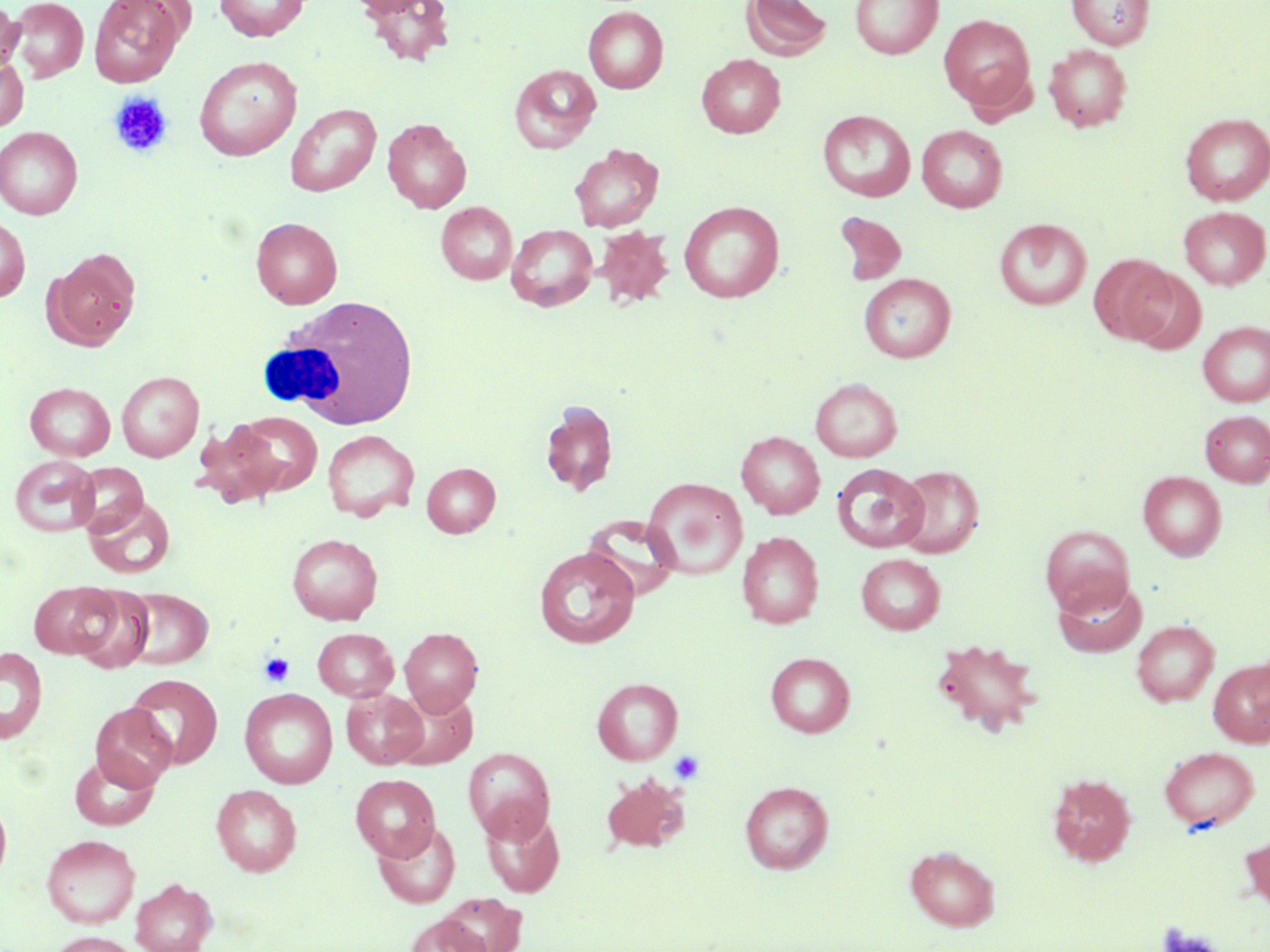

Summary:
  - Coordinate format: approximate bounding boxes as (x1, y1, x2, y2) in pixels
  - Platelet locations: (108, 91, 173, 158), (259, 652, 295, 687), (668, 750, 705, 785)
  - Uninfected red blood cell locations: (9, 0, 89, 82), (89, 0, 188, 87), (215, 0, 309, 41), (343, 0, 440, 18), (741, 0, 832, 61), (850, 0, 943, 59), (1066, 0, 1154, 50), (363, 1, 455, 67), (0, 2, 24, 76), (583, 6, 669, 93), (939, 13, 1035, 112), (1044, 44, 1132, 131), (0, 53, 28, 132), (696, 54, 786, 138), (195, 56, 301, 160), (510, 64, 601, 152), (285, 102, 381, 196), (818, 110, 915, 202), (1180, 113, 1270, 206), (382, 118, 471, 213), (917, 125, 1007, 212), (0, 126, 83, 219), (569, 143, 664, 231), (679, 201, 784, 302), (436, 202, 517, 284), (1179, 207, 1270, 289), (833, 212, 907, 286), (0, 216, 30, 302), (251, 217, 343, 308), (994, 218, 1092, 310), (506, 224, 598, 311), (593, 226, 675, 308), (45, 249, 141, 349), (1088, 254, 1176, 344), (1125, 269, 1206, 355), (860, 273, 956, 362), (1198, 321, 1270, 406), (117, 371, 204, 462), (810, 378, 902, 462), (25, 382, 116, 461), (540, 400, 618, 497), (232, 410, 323, 496), (1200, 410, 1270, 487), (193, 420, 287, 508), (322, 429, 419, 521), (736, 431, 825, 518), (8, 454, 100, 536), (71, 462, 148, 535), (422, 462, 501, 537), (832, 463, 929, 552), (893, 465, 984, 558), (1138, 471, 1226, 560), (642, 477, 748, 580), (84, 494, 176, 579), (582, 515, 681, 600), (1040, 525, 1134, 616), (737, 531, 824, 628), (287, 533, 383, 624), (534, 546, 640, 648), (856, 553, 945, 634), (1052, 576, 1148, 657), (27, 581, 119, 659), (67, 584, 155, 673), (118, 587, 213, 669), (1131, 620, 1219, 706), (312, 627, 399, 701), (399, 627, 483, 715), (930, 637, 1044, 736), (0, 646, 47, 744), (766, 652, 855, 737), (1208, 658, 1270, 747), (125, 674, 223, 769), (592, 677, 683, 765), (240, 688, 338, 788), (389, 688, 478, 770), (342, 689, 428, 769), (90, 704, 177, 791), (1159, 745, 1260, 831), (464, 747, 555, 843), (69, 752, 160, 830), (1047, 773, 1137, 866), (350, 774, 440, 861), (600, 774, 690, 854), (739, 781, 833, 874), (211, 784, 302, 876), (0, 794, 12, 885), (480, 806, 565, 897), (373, 820, 460, 908), (1240, 829, 1270, 916), (41, 833, 141, 928), (905, 846, 1000, 930), (130, 877, 218, 952), (437, 893, 527, 952), (404, 914, 492, 952), (47, 931, 142, 952)
  - White blood cell locations: (260, 296, 420, 431)
  - Slide-level diagnosis: no evidence of blood parasites
  - Image size: 1270×952 pixels
  - Stain: May-Grünwald-Giemsa
  - Preparation: thin blood smear
  - Modality: optical microscopy
  - Magnification: 1000x
  - Field of view: single